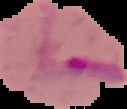

preparation = thin blood film
image type = segmented cell region on a black background
malaria status = parasitized
image size = 127×109 pixels